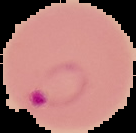
{
  "malaria_status": "parasitized",
  "image_size": "136×133 pixels",
  "preparation": "thin blood smear",
  "image_type": "segmented cell region with the area outside set to black"
}